Assess this cell for malaria.
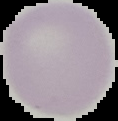

It is uninfected.

Image is 118×121 pixels. Cell region segmented out of the field of view; the surrounding area is masked to black. From a thin blood smear.